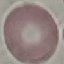

Summary:
  - Result: no malaria parasites detected
  - Capture: smartphone camera at the microscope eyepiece
  - Preparation: thin blood film
  - Image type: automatically extracted cell patch, resized to 64 × 64 pixels
  - Stain: Giemsa